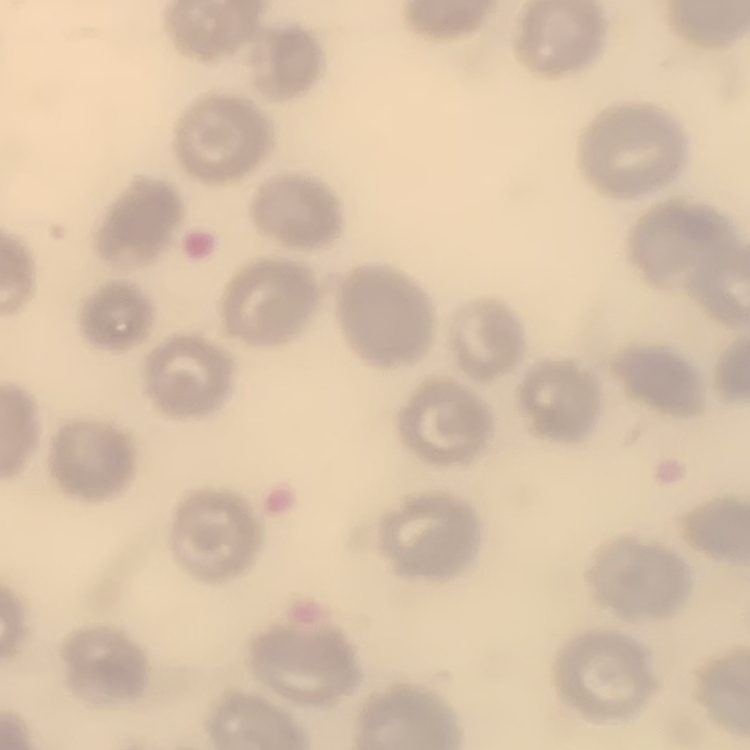 The red blood cells exhibit no rouleaux formation. Square crop of a larger photomicrograph. Thin blood smear. Field's or Giemsa stain.